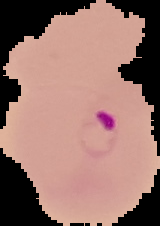
image size = 160×226 pixels
malaria status = parasitized
preparation = thin blood smear
image type = cell region segmented out of the field of view; surrounding area masked to black